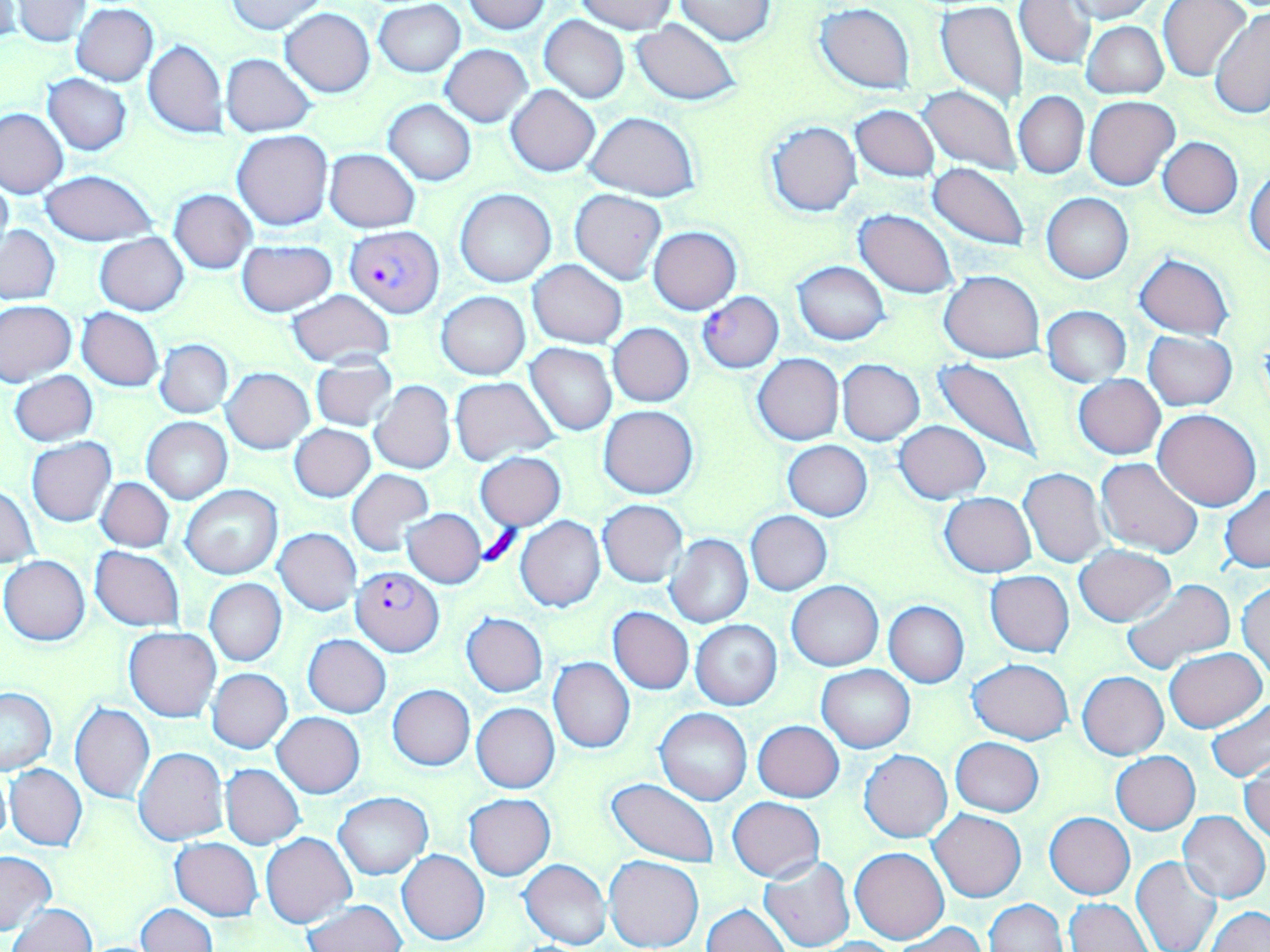

Approximate bounding boxes as [x1, y1, x2, y2] in pixels. Uninfected red blood cell locations: [223, 0, 331, 34], [465, 0, 550, 34], [573, 0, 678, 34], [675, 0, 776, 45], [1064, 0, 1158, 22], [12, 1, 93, 45], [374, 1, 465, 76], [1013, 1, 1095, 68], [1157, 1, 1253, 82], [934, 2, 1028, 105], [0, 3, 25, 41], [71, 4, 159, 86], [816, 4, 915, 92], [280, 8, 375, 97], [1210, 8, 1270, 119], [1016, 9, 1166, 79], [538, 16, 630, 102], [630, 19, 741, 106], [1081, 20, 1167, 98], [142, 40, 228, 138], [441, 44, 533, 127], [221, 54, 317, 136], [42, 74, 133, 155], [506, 84, 600, 177], [916, 85, 1023, 176], [1014, 91, 1088, 178], [1084, 96, 1178, 190], [383, 99, 477, 186], [851, 105, 939, 182], [0, 108, 67, 197], [584, 111, 701, 199], [763, 120, 862, 217], [232, 131, 332, 231], [1158, 137, 1243, 217], [324, 149, 419, 232], [927, 162, 1030, 250], [1246, 169, 1270, 261], [0, 171, 14, 256], [39, 171, 158, 245], [455, 188, 556, 288], [569, 188, 666, 285], [168, 189, 256, 274], [1041, 193, 1133, 283], [853, 209, 959, 298], [2, 224, 60, 305], [649, 226, 742, 313], [94, 233, 189, 314], [236, 241, 337, 317], [1134, 253, 1233, 339], [792, 260, 891, 345], [528, 261, 626, 349], [940, 270, 1045, 361], [287, 291, 395, 366], [437, 291, 529, 380], [1, 301, 77, 385], [1042, 305, 1130, 386], [76, 308, 163, 392], [608, 322, 694, 407], [1144, 331, 1237, 410], [155, 339, 233, 418], [525, 343, 617, 436], [752, 354, 843, 444], [309, 355, 398, 432], [934, 355, 1045, 462], [836, 359, 925, 445], [221, 369, 314, 453], [9, 370, 98, 446], [1073, 374, 1166, 459], [449, 376, 559, 465], [369, 381, 456, 474], [599, 405, 699, 499], [1154, 408, 1261, 510], [142, 417, 231, 503], [895, 420, 989, 502], [289, 424, 375, 502], [26, 437, 116, 527], [783, 441, 873, 521], [474, 452, 566, 530], [1096, 456, 1204, 558], [347, 468, 433, 557], [1018, 468, 1107, 567], [97, 476, 174, 552], [1, 484, 40, 569], [1221, 484, 1270, 572], [181, 485, 282, 579], [940, 492, 1035, 577], [599, 500, 687, 587], [402, 509, 486, 588], [746, 511, 832, 595], [516, 516, 605, 613], [274, 528, 361, 616], [664, 533, 752, 629], [1075, 544, 1175, 627], [90, 547, 185, 630], [0, 556, 90, 645], [985, 569, 1075, 658], [204, 578, 286, 667], [1120, 578, 1236, 677], [1237, 580, 1270, 679], [788, 581, 883, 670], [883, 601, 969, 687], [608, 606, 694, 695], [461, 613, 548, 697], [690, 619, 781, 710], [123, 626, 221, 722], [302, 635, 391, 718], [1163, 647, 1266, 732], [548, 657, 635, 753], [968, 658, 1074, 745], [817, 664, 915, 753], [207, 669, 292, 753], [1077, 672, 1168, 759], [388, 684, 475, 770], [0, 687, 55, 775], [1205, 697, 1270, 783], [70, 703, 155, 804], [471, 703, 559, 793], [655, 708, 751, 806], [273, 712, 365, 797], [753, 720, 843, 802], [950, 737, 1044, 817], [134, 748, 228, 847], [859, 749, 952, 842], [1111, 751, 1200, 833], [1240, 758, 1270, 845], [6, 763, 88, 852], [221, 764, 305, 849], [0, 767, 11, 851], [604, 777, 719, 867], [334, 792, 431, 880], [464, 793, 555, 880], [728, 797, 825, 881], [928, 809, 1026, 902], [1178, 810, 1268, 901], [1045, 813, 1135, 899], [261, 832, 356, 928], [170, 838, 262, 921], [850, 846, 948, 944], [0, 850, 57, 936], [397, 850, 488, 945], [604, 854, 703, 951], [759, 855, 855, 952], [1131, 856, 1222, 952], [519, 858, 611, 950], [983, 899, 1067, 951], [1064, 899, 1152, 952], [303, 900, 406, 951], [136, 902, 217, 952], [9, 903, 96, 952], [701, 903, 791, 952], [1205, 906, 1270, 952], [897, 923, 986, 952], [813, 936, 905, 952]. Platelet locations: [477, 524, 524, 571]. Plasmodium falciparum-infected red blood cell locations: [344, 226, 442, 317], [697, 292, 784, 372], [351, 567, 445, 656]. Slide-level diagnosis: Plasmodium falciparum. Image is 1270×952 pixels. Captured at 1000x magnification. Light microscopy. Thin blood film. May-Grünwald-Giemsa-stained preparation. One field of a larger specimen.